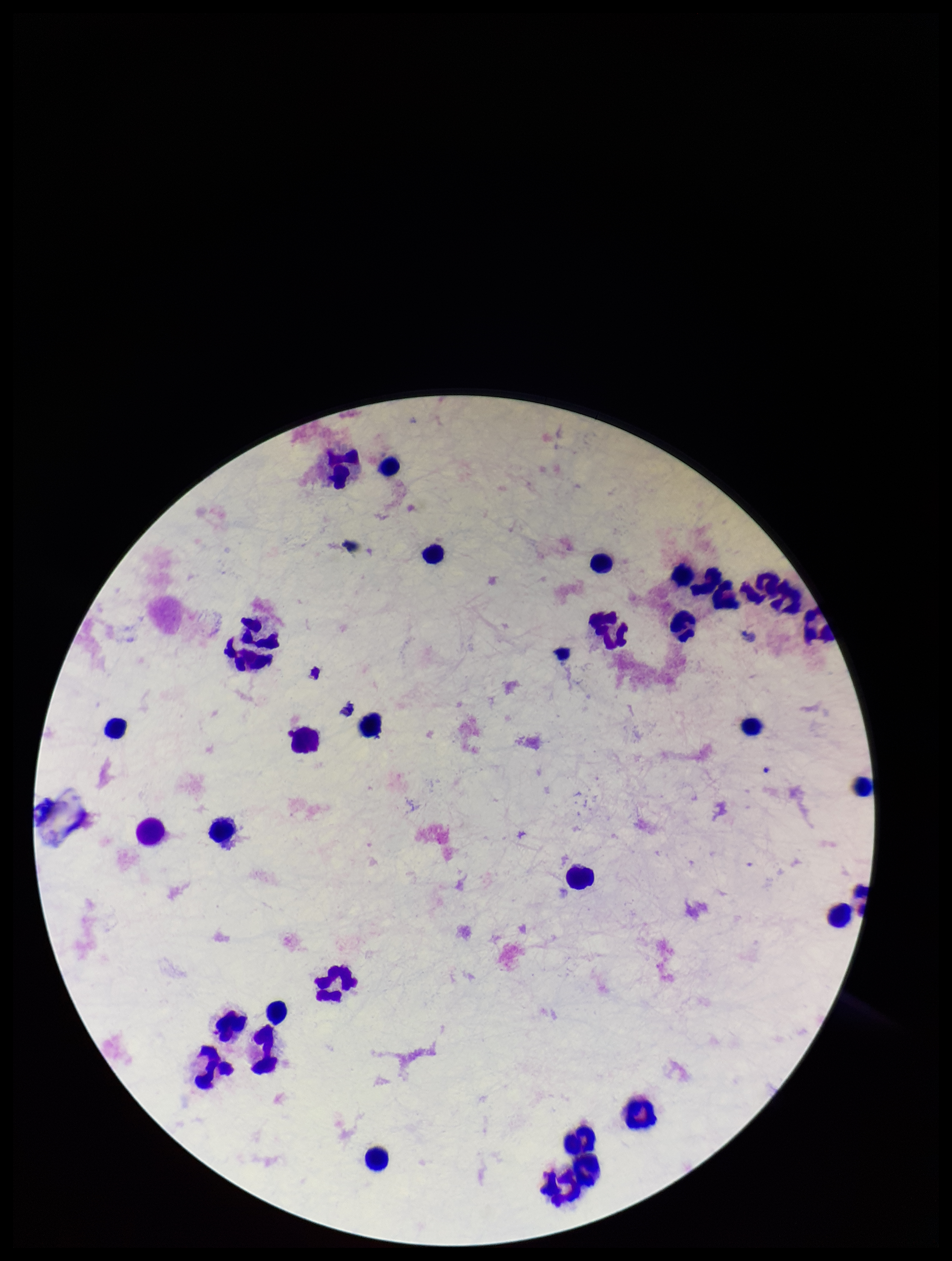

{
  "field_of_view": "one from this slide",
  "plasmodium_parasites": "none identified",
  "leukocyte_count": 31,
  "parasite_count": 0,
  "capture": "smartphone photograph through the microscope eyepiece",
  "patient_malaria_status": "negative",
  "stain": "Giemsa",
  "preparation": "thick",
  "image_size": "952×1261 pixels"
}